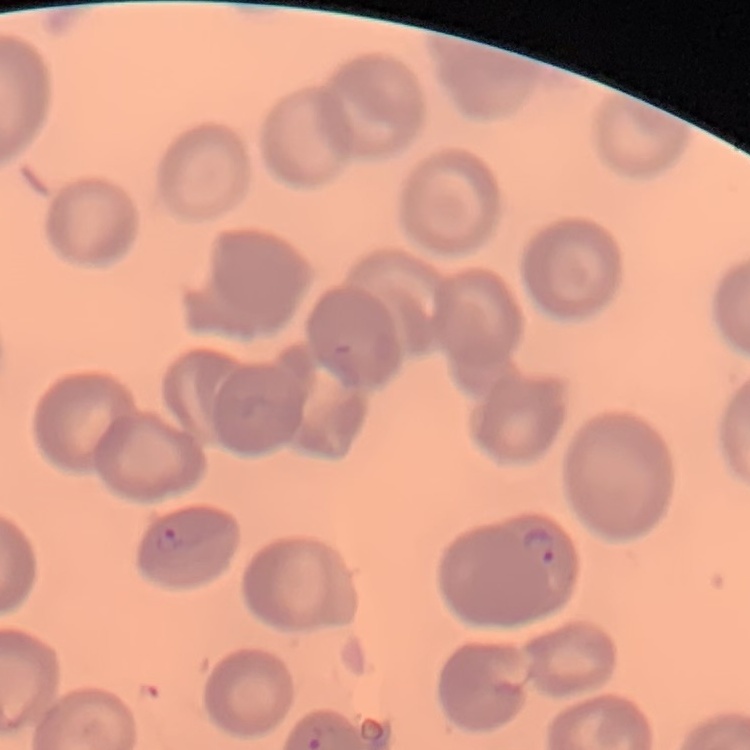
Summary:
  - Red blood cell morphology: no rouleaux formation
  - Preparation: thin peripheral smear
  - Stain: Field's or Giemsa
  - Image type: one tile cut from a larger photomicrograph